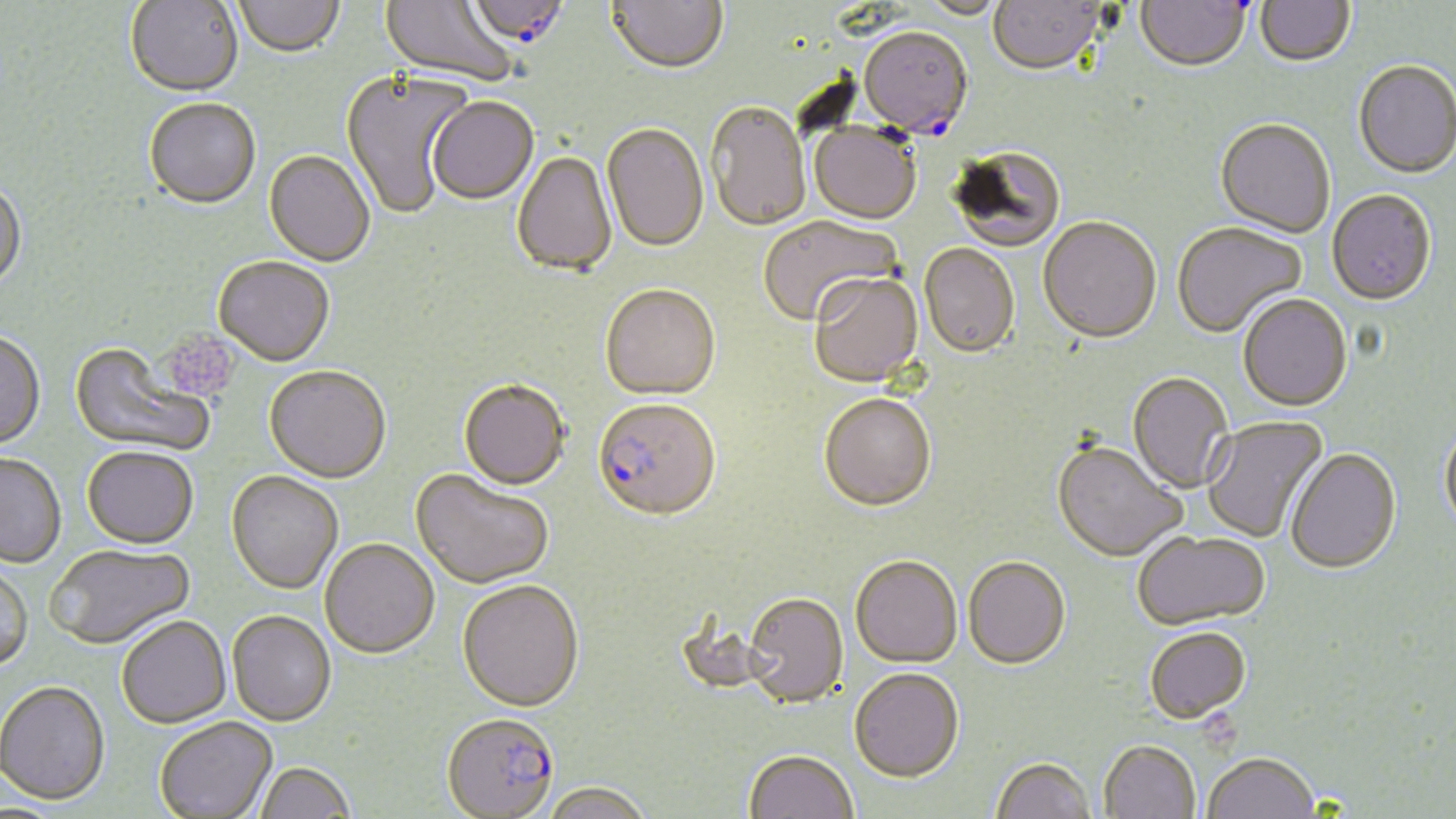

Approximate bounding boxes as (x1,y1)-(x2,y2) corner pairs in pixels. Platelet locations: (165,322)-(241,404), (1201,715)-(1243,755). Uninfected red blood cell locations: (125,0)-(243,99), (380,0)-(518,89), (606,0)-(728,77), (989,0)-(1105,78), (1136,0)-(1250,75), (1255,0)-(1355,70), (234,1)-(345,60), (914,1)-(1009,21), (1354,62)-(1455,181), (340,70)-(472,222), (428,99)-(539,206), (144,100)-(261,212), (707,105)-(811,234), (1214,120)-(1335,240), (809,124)-(920,226), (601,125)-(708,255), (951,147)-(1066,255), (263,152)-(375,268), (512,152)-(618,279), (0,180)-(26,295), (1327,192)-(1437,309), (758,216)-(902,328), (1038,219)-(1161,346), (1172,224)-(1308,340), (919,245)-(1020,360), (213,258)-(335,368), (810,275)-(923,389), (600,287)-(720,404), (1238,296)-(1353,414), (0,331)-(46,451), (69,343)-(213,458), (264,367)-(391,485), (1128,373)-(1233,495), (458,382)-(570,493), (819,396)-(937,514), (1201,415)-(1329,543), (1440,423)-(1456,537), (1052,444)-(1187,565), (82,447)-(199,550), (1285,450)-(1402,577), (0,453)-(66,569), (226,471)-(343,595), (410,471)-(553,591), (1133,533)-(1269,632), (320,540)-(439,660), (47,542)-(197,651), (850,559)-(962,670), (963,559)-(1071,673), (0,561)-(34,673), (457,582)-(584,715), (742,595)-(848,710), (227,612)-(336,728), (117,617)-(231,729), (1145,630)-(1251,728), (850,671)-(964,785), (0,681)-(110,806), (155,718)-(277,819), (1099,743)-(1200,819), (745,753)-(858,819), (1203,756)-(1320,818), (991,759)-(1097,819), (254,764)-(355,819), (540,785)-(654,819). Plasmodium falciparum-infected red blood cell locations: (466,0)-(571,53), (857,29)-(973,142), (592,402)-(720,526), (441,716)-(558,819). Slide-level diagnosis: Plasmodium falciparum. May-Grünwald-Giemsa-stained preparation. Image is 1456×819 pixels. Thin blood film. 1000x magnification. Single field of view. Optical microscopy.